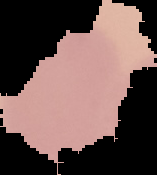
Image is 157×175 pixels. Malaria status: uninfected. The area outside the segmented cell region is set to black. From a thin blood film.